Report the malaria status of this cell.
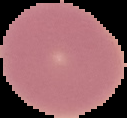

Uninfected.

From a thin blood smear. Image is 127×118 pixels. Cell region segmented out of the field of view; the surrounding area is masked to black.